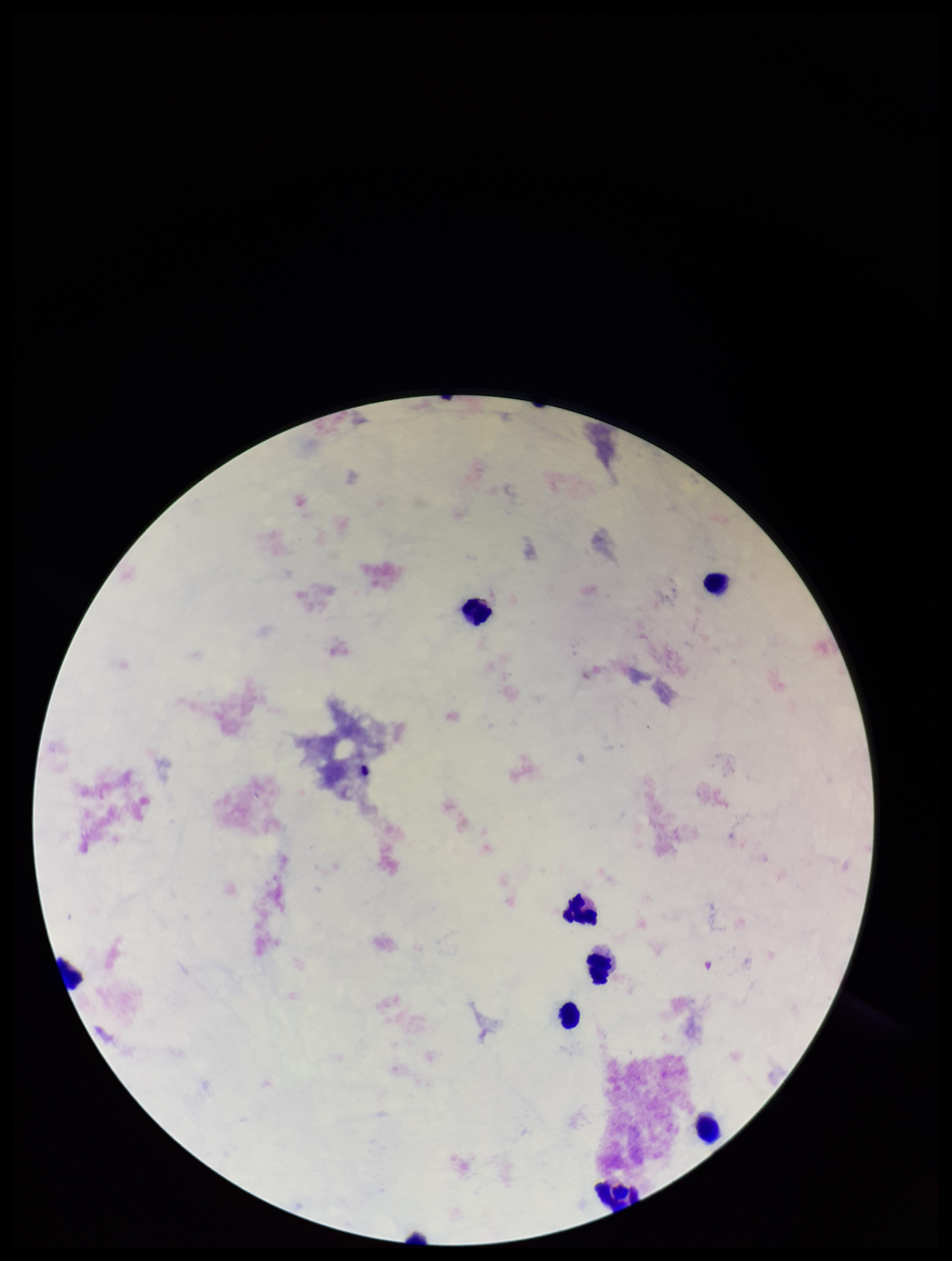

Summary:
  - Leukocyte count: 8
  - Capture: smartphone photograph through the microscope eyepiece
  - Plasmodium parasites: none identified
  - Patient malaria status: negative
  - Field of view: one from this slide
  - Stain: Giemsa
  - Image size: 952×1261 pixels
  - Parasite count: 0
  - Preparation: thick blood smear